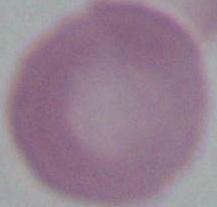
{
  "modality": "photomicrograph",
  "magnification": "1000x",
  "identification": "erythrocyte"
}